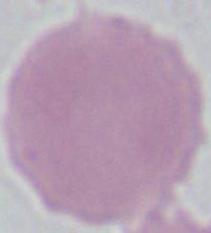

magnification = 1000x
modality = photomicrograph
identification = red blood cell